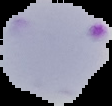 Result: Plasmodium parasites detected. Cell region segmented out of the field of view; the surrounding area is masked to black. From a thin blood smear. Image is 112×106 pixels.